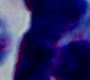

Summary:
  - Identification: leukocyte
  - Modality: photomicrograph
  - Magnification: 1000x